Assess this cell for malaria.
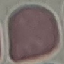
It is uninfected.

{
  "capture": "smartphone camera at the microscope eyepiece",
  "image_type": "automatically extracted cell patch, resized to 64 × 64 pixels",
  "stain": "Giemsa",
  "preparation": "thin smear"
}